State the blood parasite species.
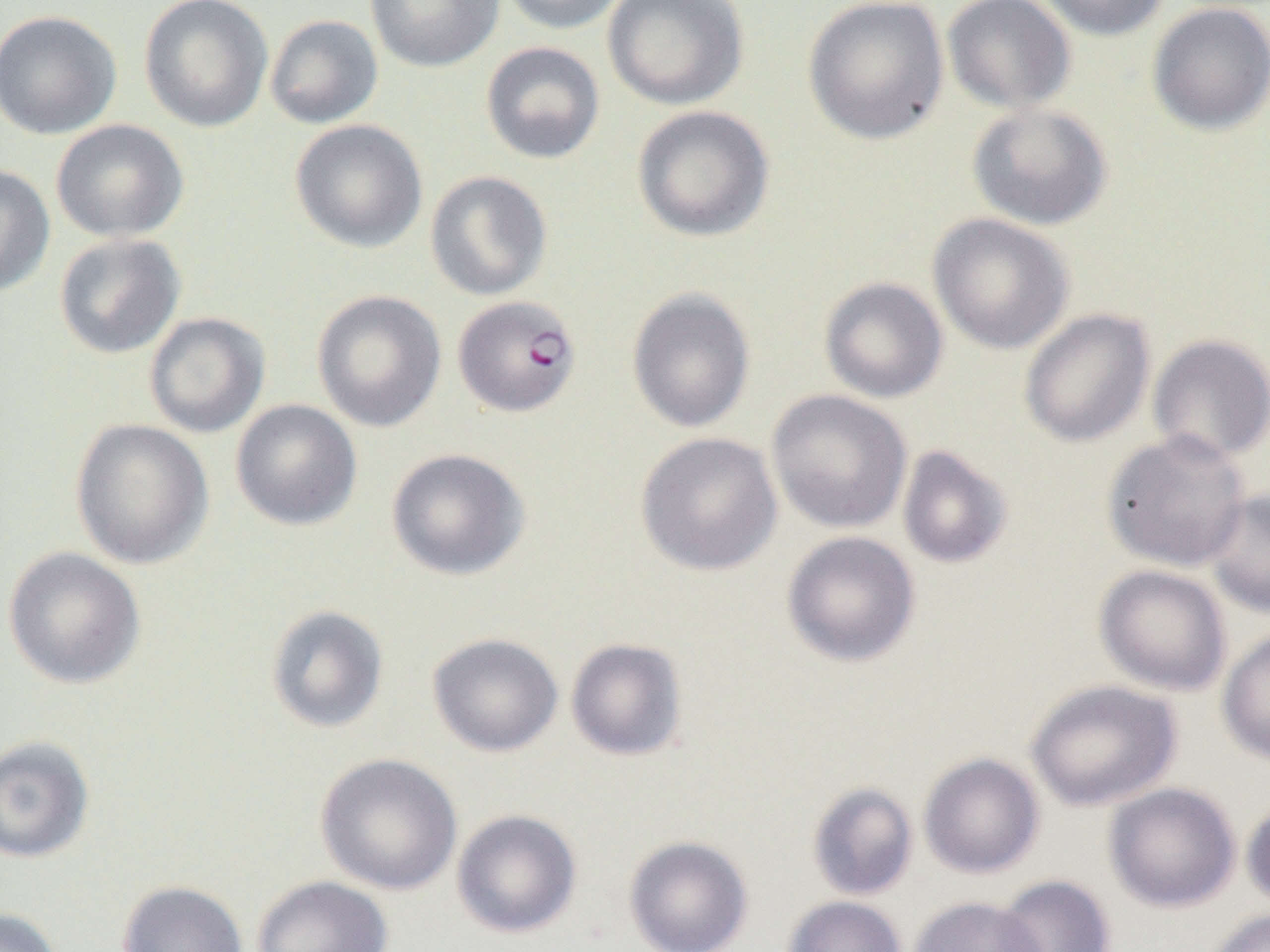

Plasmodium falciparum.

Summary:
  - Coordinate format: approximate bounding boxes as (x1,y1)-(x2,y2) corner pairs in pixels
  - Uninfected red blood cell locations: (138,0)-(273,133), (364,0)-(504,72), (499,0)-(631,34), (602,0)-(749,110), (802,0)-(950,145), (941,0)-(1077,115), (1034,0)-(1172,41), (1147,2)-(1270,136), (0,9)-(122,140), (264,14)-(383,129), (480,41)-(606,164), (966,103)-(1113,231), (632,105)-(775,242), (50,119)-(189,243), (289,119)-(428,253), (0,163)-(55,296), (425,170)-(553,301), (927,213)-(1075,354), (53,233)-(187,359), (819,277)-(949,403), (626,288)-(756,433), (310,290)-(446,432), (1018,308)-(1156,448), (143,312)-(270,438), (1147,333)-(1270,464), (766,389)-(912,534), (230,399)-(363,531), (70,418)-(214,570), (1102,429)-(1252,572), (635,431)-(783,576), (897,445)-(1014,569), (386,447)-(530,581), (1204,489)-(1270,619), (781,530)-(921,667), (2,547)-(147,689), (1094,564)-(1232,696), (265,604)-(390,733), (1217,627)-(1270,766), (427,632)-(564,757), (565,638)-(688,761), (1025,679)-(1182,811), (0,735)-(96,864), (918,752)-(1045,879), (315,753)-(463,895), (807,782)-(919,901), (1103,782)-(1241,913), (1241,795)-(1270,913), (451,809)-(582,939), (623,835)-(754,952), (993,874)-(1116,952), (251,875)-(393,952), (116,880)-(249,952), (782,895)-(907,952), (909,896)-(1047,952), (0,907)-(64,952), (1205,908)-(1270,952)
  - Plasmodium falciparum-infected red blood cell locations: (453,294)-(581,417)
  - Image size: 1270×952 pixels
  - Preparation: thin blood smear
  - Modality: optical microscopy
  - Magnification: 1000x
  - Field of view: one of a larger specimen